Classify this cell by malaria status.
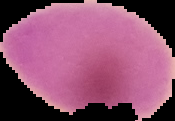
Uninfected.

Summary:
  - Image type: segmented cell region on a black background
  - Image size: 175×121 pixels
  - Preparation: thin blood film